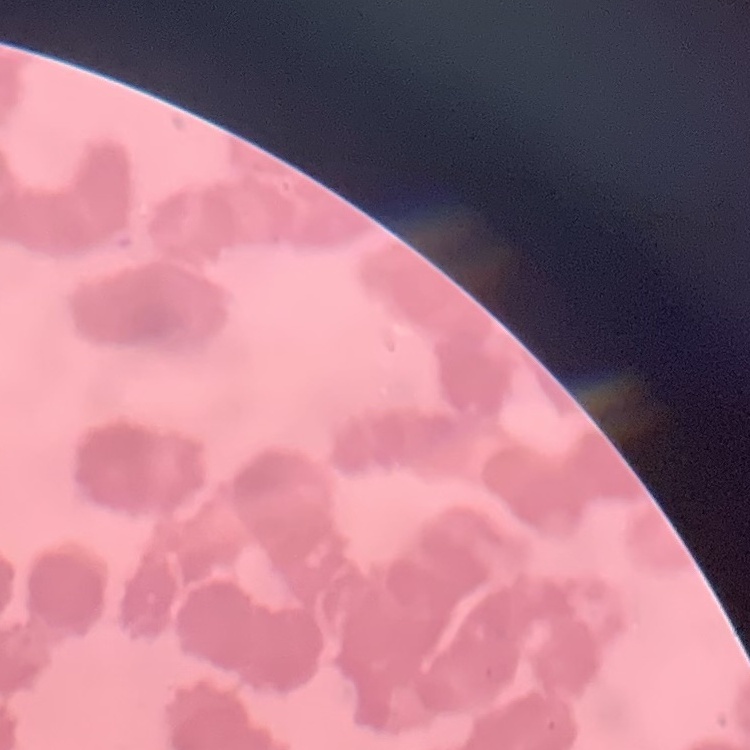
The erythrocytes exhibit rouleaux formation. Thin blood film. Stained with either Field's or Giemsa. Square crop of a larger photomicrograph.